Assess the morphology of the red blood cells.
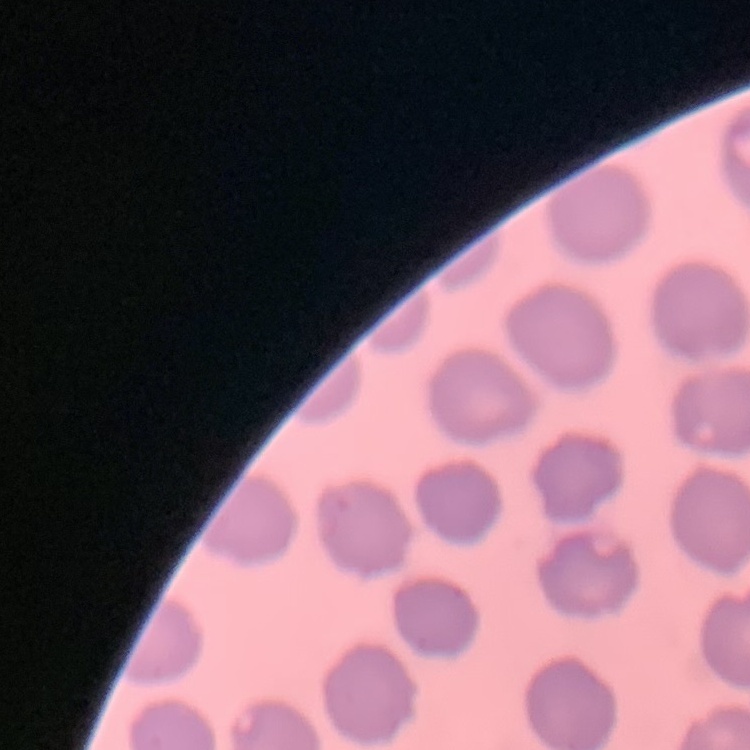

No rouleaux formation.

Summary:
  - Preparation: thin peripheral smear
  - Image type: one tile cut from a larger photomicrograph
  - Stain: Field's or Giemsa